Identify the parasite.
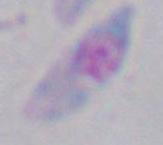
This is Toxoplasma gondii.

Captured at 1000x magnification. Micrograph.